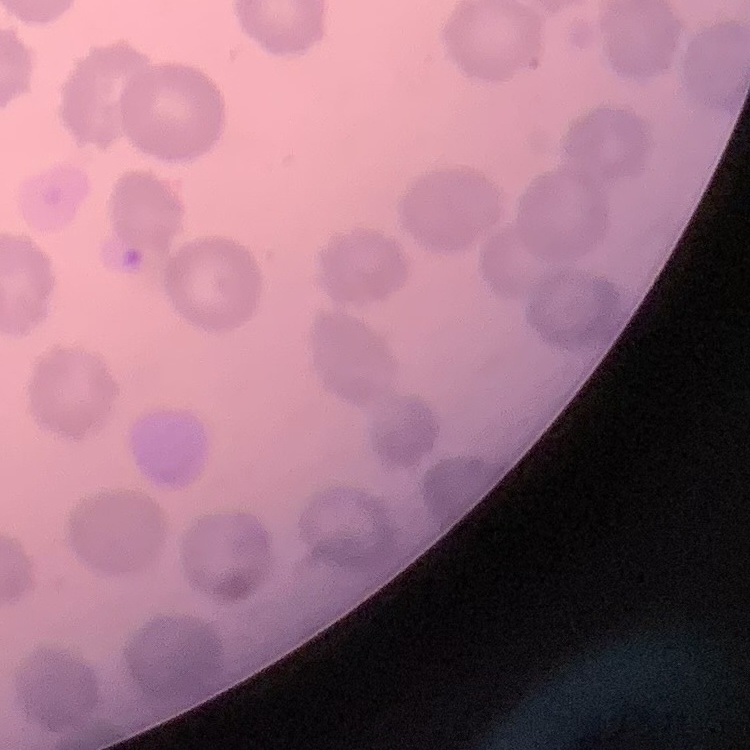

red blood cell morphology = no rouleaux formation
stain = Field's or Giemsa
image type = square crop of a larger photomicrograph
preparation = thin peripheral smear